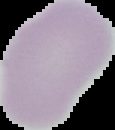

image size = 115×130 pixels
preparation = thin blood film
malaria status = uninfected
image type = cell region segmented out of the field of view; surrounding area masked to black